State which parasite is depicted.
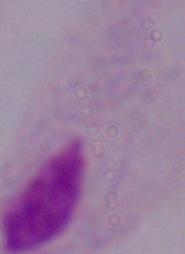
This is a trichomonad.

Summary:
  - Modality: photomicrograph
  - Magnification: 1000x